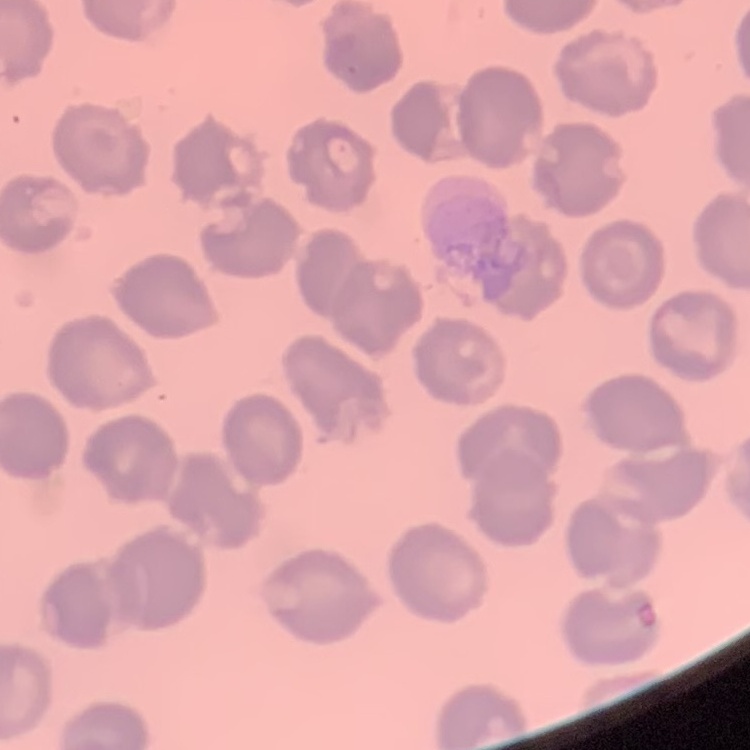
erythrocyte morphology = no rouleaux formation
preparation = thin blood film
image type = one tile cut from a larger photomicrograph
stain = Field's or Giemsa